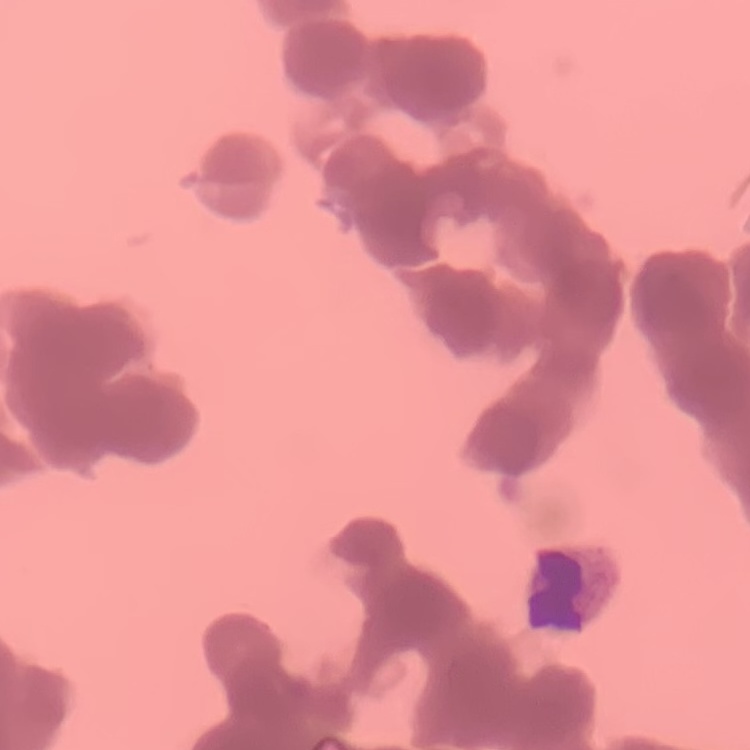

Summary:
  - Red blood cell morphology: rouleaux formation
  - Stain: Field's or Giemsa
  - Preparation: thin blood film
  - Image type: one tile cut from a larger photomicrograph